Name the blood parasite species.
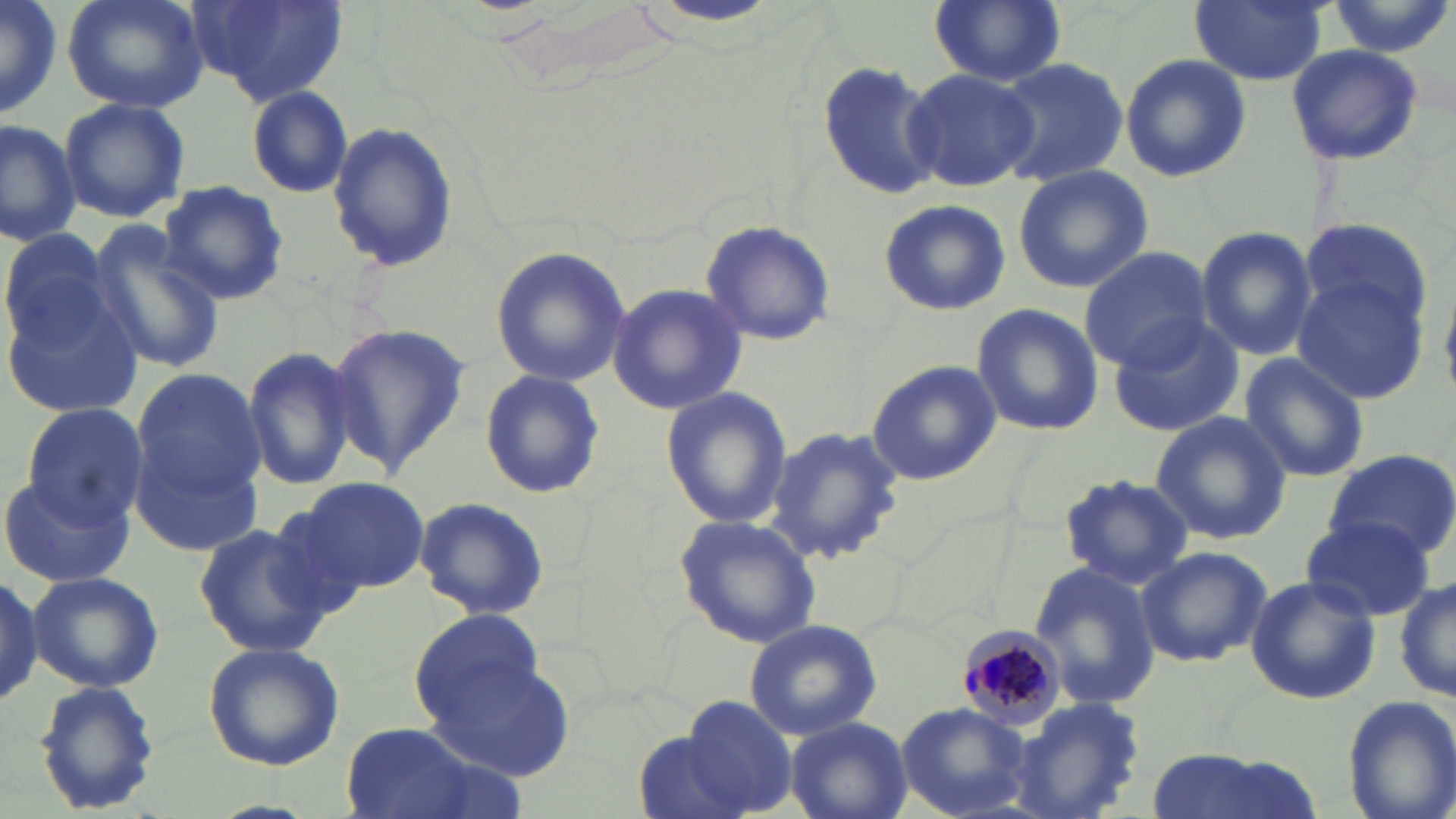

Plasmodium malariae.

{
  "field_of_view": "single",
  "modality": "light microscopy",
  "image_size": "1456×819 pixels",
  "preparation": "thin blood smear",
  "magnification": "1000x",
  "stain": "May-Grünwald-Giemsa",
  "plasmodium_malariae_infected_red_blood_cell_locations": "approximate bounding boxes as (x1, y1, x2, y2) in pixels: (952, 624, 1069, 731)",
  "uninfected_red_blood_cell_locations": "approximate bounding boxes as (x1, y1, x2, y2) in pixels: (0, 0, 65, 121), (62, 0, 208, 113), (185, 0, 350, 106), (1187, 0, 1329, 85), (928, 1, 1065, 88), (1325, 1, 1454, 56), (644, 2, 782, 30), (1285, 44, 1425, 166), (1119, 53, 1250, 183), (815, 57, 943, 201), (989, 57, 1130, 189), (902, 66, 1037, 196), (245, 85, 354, 199), (58, 96, 190, 220), (0, 118, 81, 247), (327, 121, 457, 273), (1013, 164, 1152, 293), (157, 181, 290, 305), (878, 198, 1011, 316), (1298, 218, 1431, 329), (699, 220, 837, 347), (85, 223, 226, 374), (0, 225, 115, 350), (1195, 225, 1319, 361), (489, 245, 630, 389), (1079, 247, 1215, 369), (1291, 275, 1429, 405), (1, 282, 149, 422), (607, 282, 749, 417), (970, 303, 1103, 436), (1106, 316, 1245, 439), (322, 323, 470, 479), (240, 344, 359, 492), (1239, 353, 1370, 483), (866, 360, 999, 486), (124, 368, 267, 551), (478, 370, 606, 501), (659, 385, 791, 529), (20, 403, 148, 530), (1149, 411, 1292, 545), (761, 427, 907, 565), (1322, 449, 1456, 562), (2, 471, 131, 587), (1058, 473, 1194, 589), (293, 475, 433, 594), (413, 495, 550, 621), (673, 514, 821, 649), (1301, 515, 1436, 622), (192, 518, 343, 660), (1135, 545, 1272, 668), (1027, 561, 1162, 709), (28, 571, 164, 692), (1244, 574, 1381, 705), (1393, 575, 1456, 706), (411, 609, 547, 724), (744, 618, 882, 739), (202, 641, 345, 770), (426, 648, 576, 783), (33, 679, 161, 817), (1340, 694, 1456, 819), (675, 696, 799, 817), (1009, 698, 1152, 819), (896, 703, 1035, 818), (785, 716, 912, 819), (341, 725, 488, 817), (634, 728, 752, 819), (1144, 750, 1324, 819)"
}